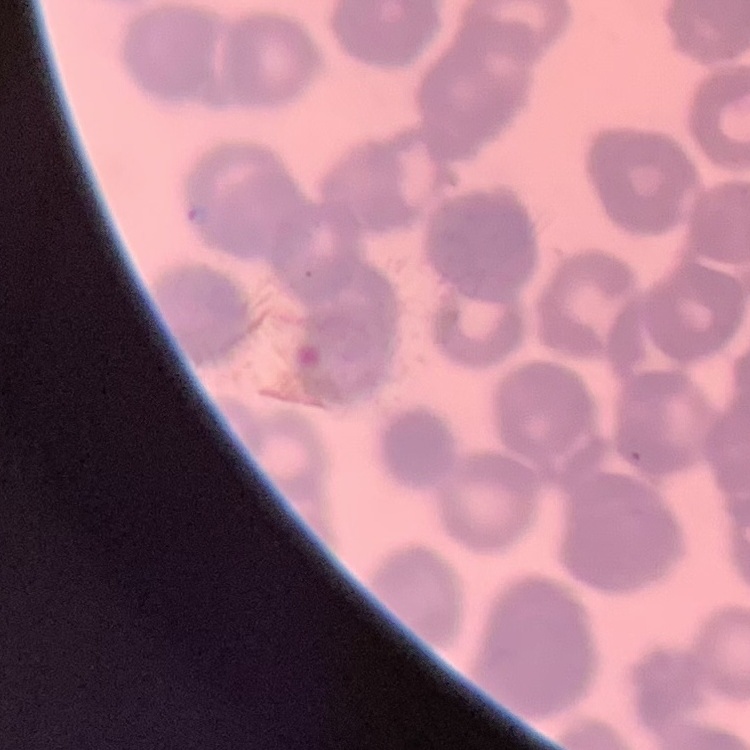
Summary:
  - Red blood cell morphology: rouleaux formation
  - Stain: Field's or Giemsa
  - Preparation: thin blood film
  - Image type: one tile cut from a larger photomicrograph